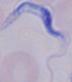

magnification = 1000x
identification = trypanosome
modality = micrograph